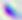

Captured at 400x magnification. Toxoplasma gondii is seen. Micrograph.